Identify the parasite.
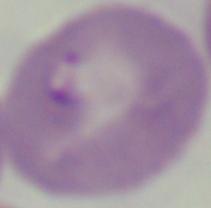

Babesia.

Captured at 1000x magnification. Micrograph.